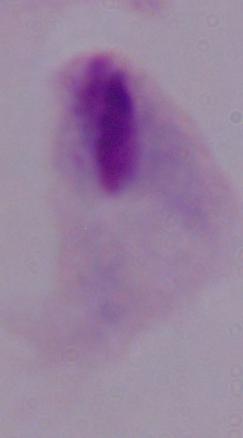 Micrograph. A trichomonad is seen. 1000x magnification.